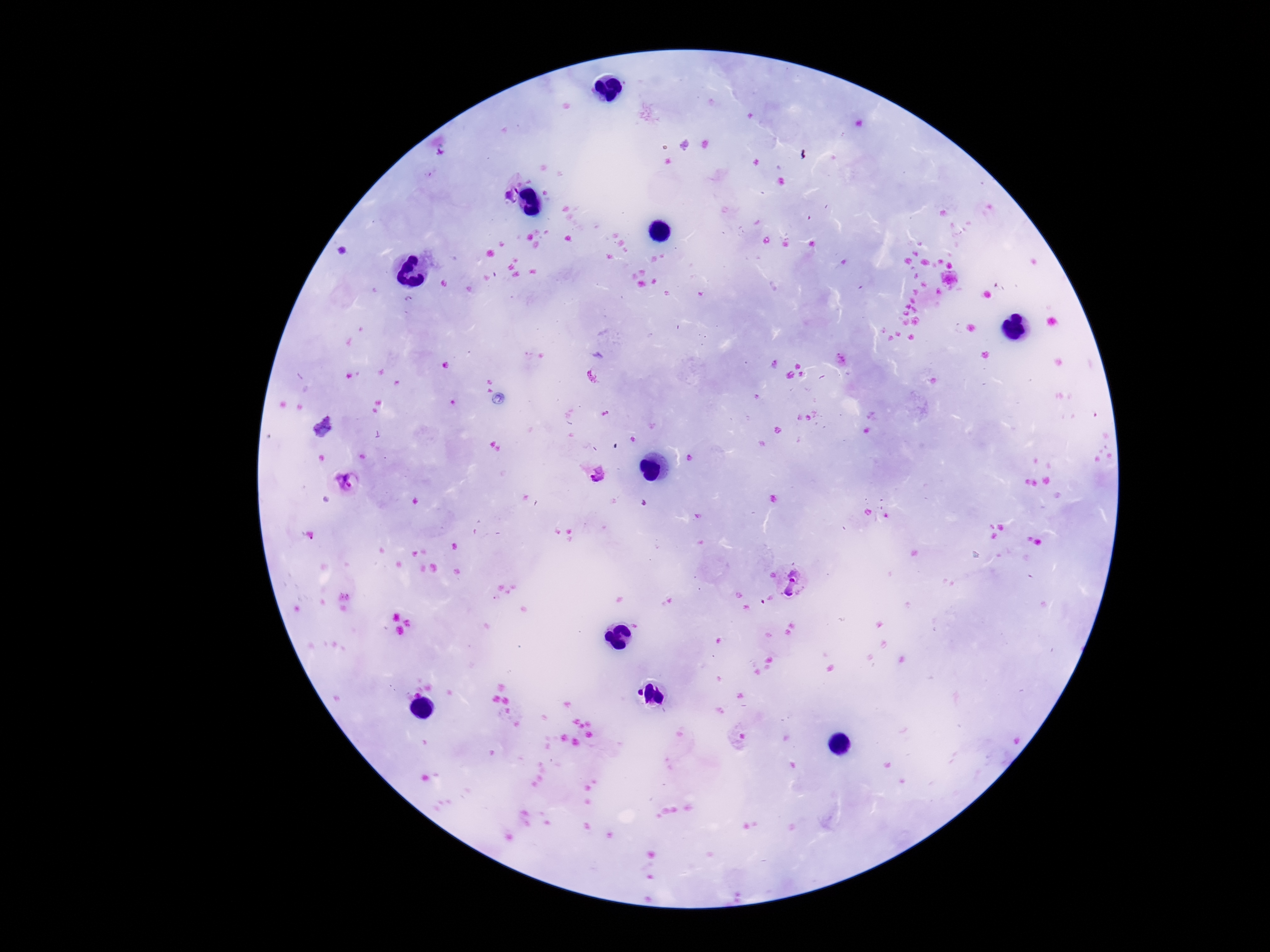

Approximate centers as {x, y} in pixels.
Summary:
  - Plasmodium parasite locations: {507, 191}, {593, 471}, {348, 481}, {792, 582}
  - Image size: 1270×952 pixels
  - Stain: Giemsa
  - Field of view: single
  - Capture: smartphone camera through the microscope eyepiece
  - Preparation: thick peripheral-blood smear
  - Magnification: 100x
  - Patient malaria status: infected